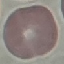
Malaria status: uninfected. Acquired by smartphone through the microscope eyepiece. Thin blood smear. Giemsa stain. Cell patch, automatically extracted from a larger field of view and resized to 64 × 64 pixels.